Give the position of every Plasmodium parasite visible.
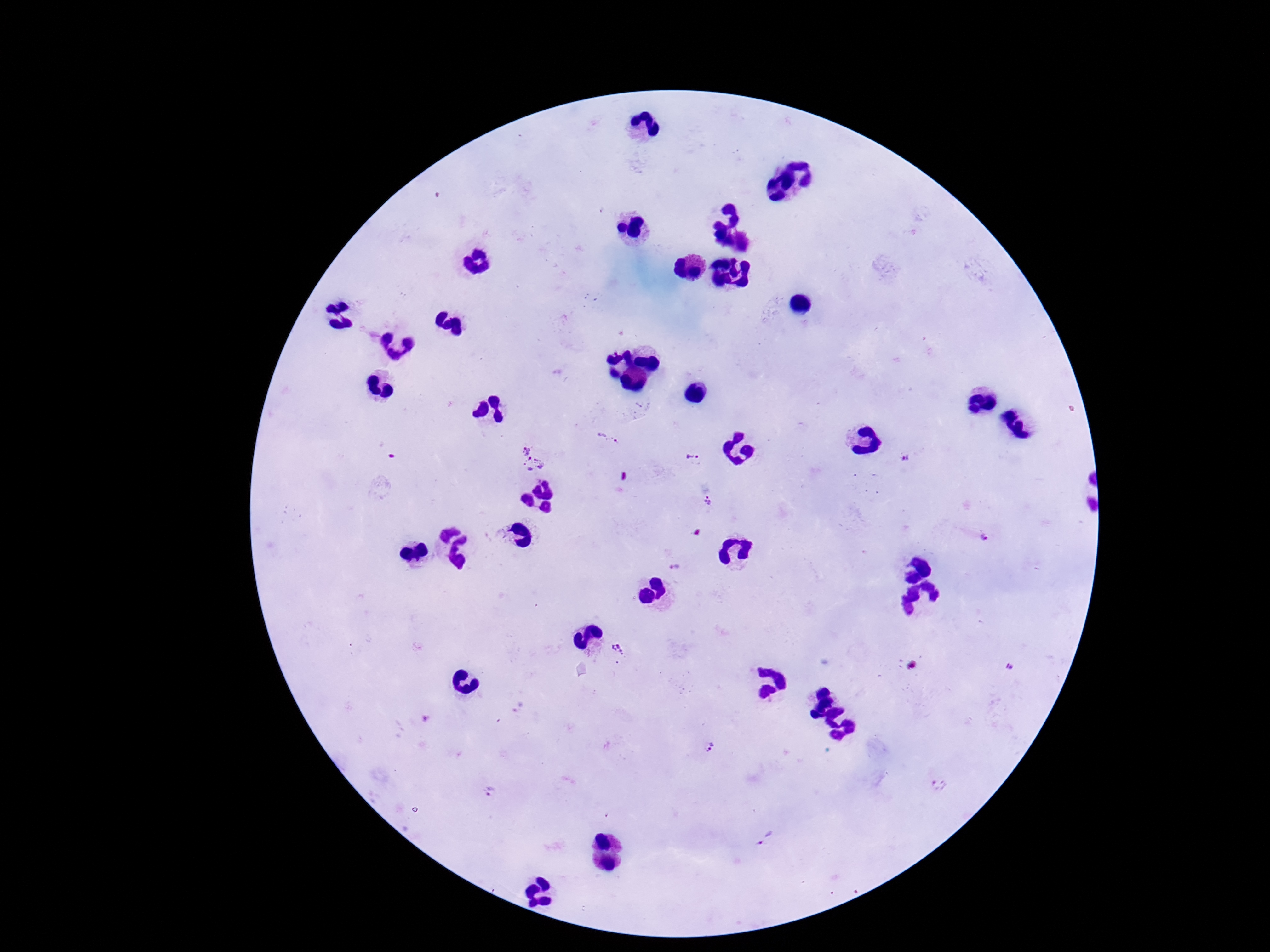
Approximate centers as [x, y] in pixels.
Plasmodium parasites: [607, 437], [526, 446], [692, 457], [906, 460], [534, 466], [707, 501], [987, 537], [675, 566], [619, 650], [1009, 666], [709, 748], [940, 784], [489, 792], [765, 837].

stain: Giemsa
preparation: thick peripheral-blood smear
magnification: 100x
capture: smartphone camera through the microscope eyepiece
image_size: 1270×952 pixels
field_of_view: single
patient_malaria_status: positive